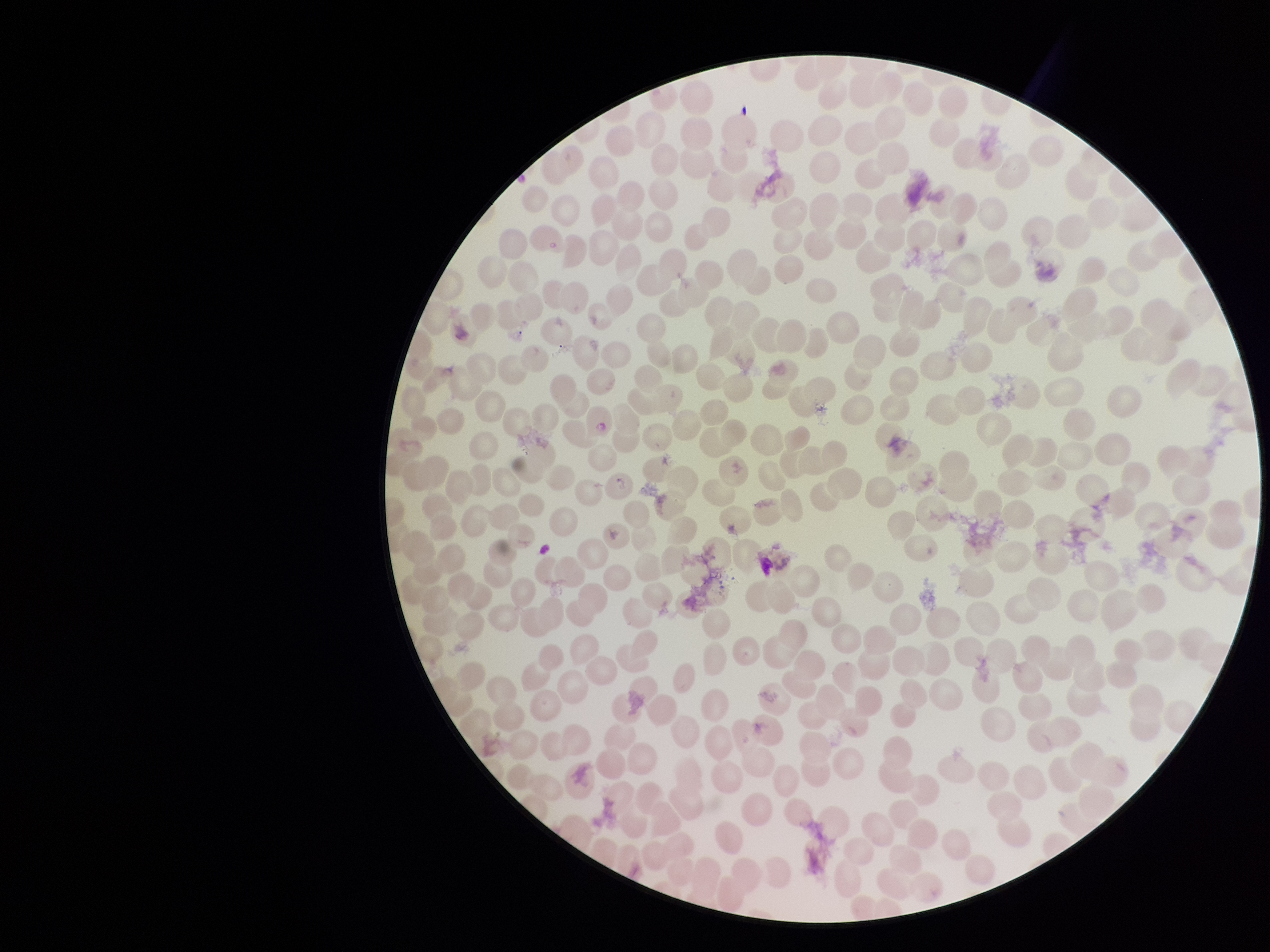
stain = Giemsa
field of view = single
capture = smartphone photograph through the microscope eyepiece
red blood cell count = 311
parasitized red blood cell count = 0
patient malaria status = negative
preparation = thin smear
image size = 1270×952 pixels
parasitized red blood cells = none identified